Give a bounding box for every leukocyte visible.
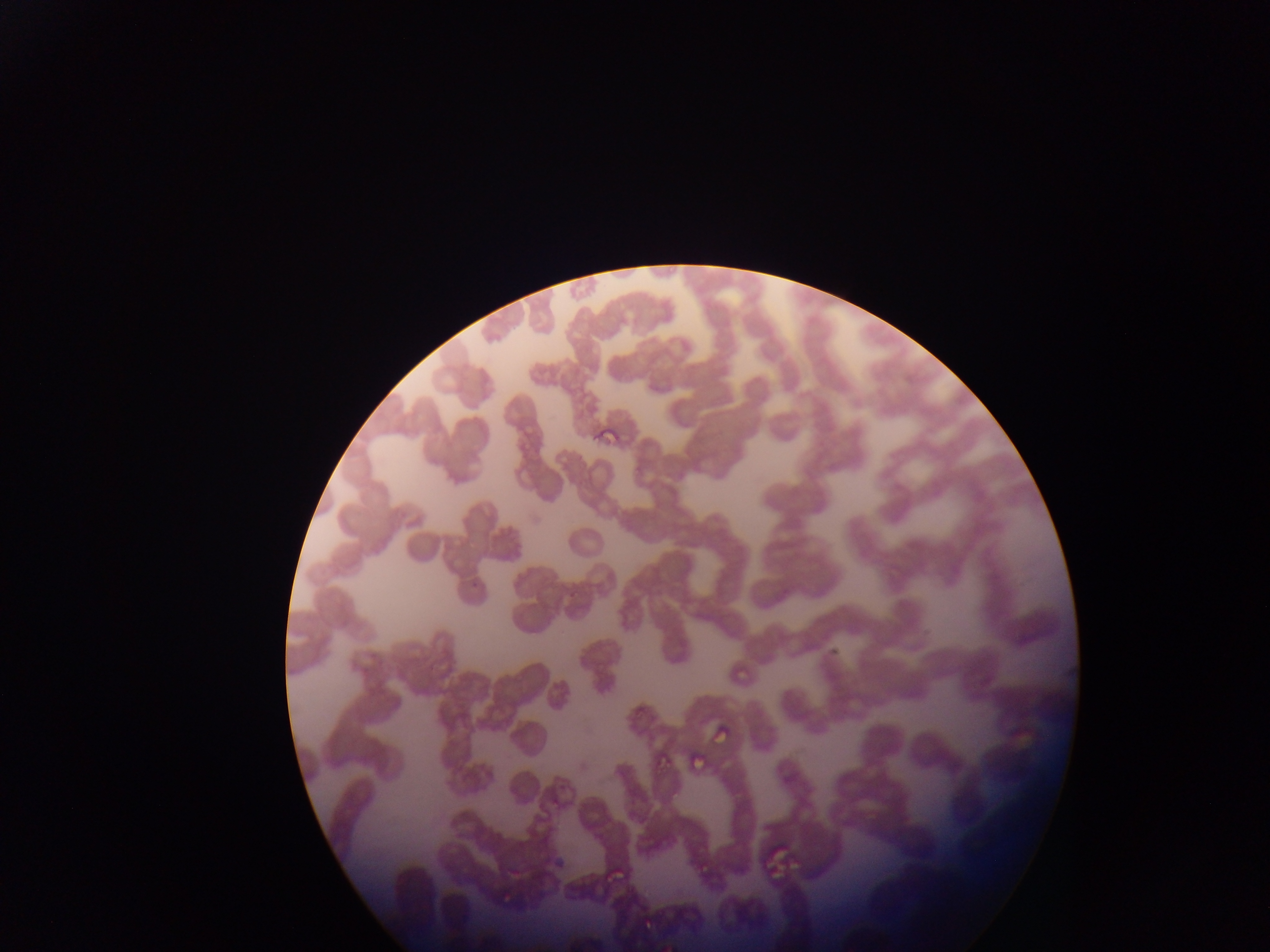
No leukocytes observed.

Approximate bounding boxes as (left, top, right, bottom) in pixels. Malaria parasite locations: (592, 423, 622, 443), (732, 661, 750, 681), (1008, 707, 1038, 749), (706, 724, 727, 744), (650, 745, 682, 769), (694, 755, 704, 773), (775, 760, 795, 782), (725, 786, 743, 805), (653, 823, 665, 843), (761, 832, 803, 875), (693, 853, 720, 871), (605, 858, 629, 879), (633, 909, 668, 929). Collected in Ghana. Image is 1270×952 pixels. Photographed through a microscope with a mobile-phone camera. Thin blood film. One field of view.